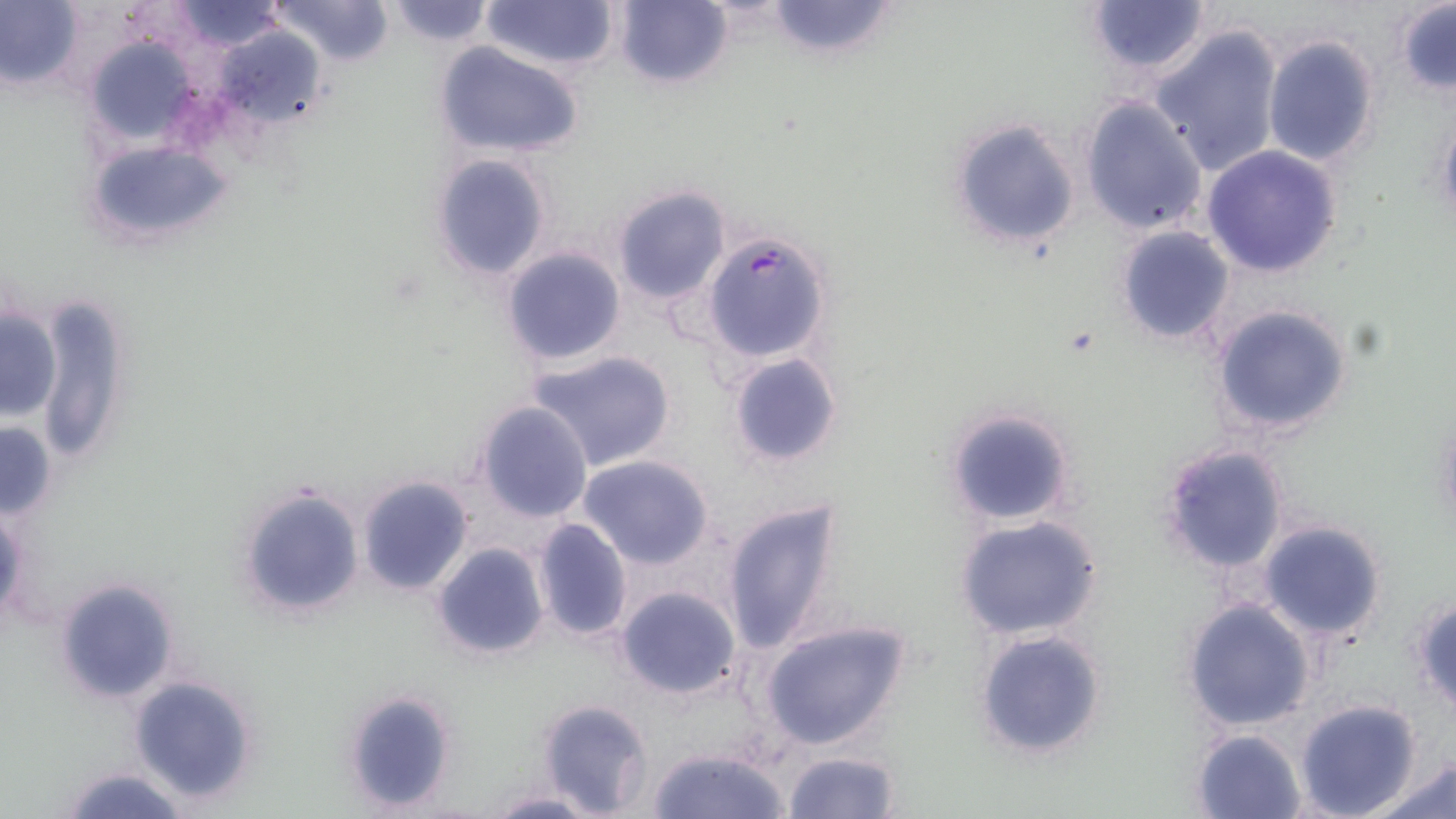

{
  "slide_level_diagnosis": "Plasmodium falciparum",
  "uninfected_red_blood_cell_locations": "approximate bounding boxes as (x1, y1, x2, y2) in pixels: (168, 0, 289, 53), (268, 0, 397, 68), (385, 0, 494, 47), (478, 0, 621, 72), (612, 0, 732, 89), (761, 0, 902, 60), (0, 1, 83, 90), (1084, 2, 1214, 80), (1394, 2, 1456, 93), (1151, 25, 1283, 175), (211, 26, 328, 124), (80, 34, 197, 146), (1261, 34, 1381, 169), (434, 43, 584, 159), (1079, 97, 1209, 237), (1433, 105, 1456, 229), (945, 116, 1082, 253), (85, 140, 234, 248), (1201, 146, 1344, 278), (430, 152, 553, 282), (612, 185, 731, 305), (1114, 225, 1236, 345), (501, 247, 627, 366), (33, 294, 135, 469), (1208, 303, 1356, 438), (0, 308, 61, 421), (527, 349, 677, 470), (726, 352, 844, 467), (476, 400, 593, 521), (941, 405, 1076, 530), (0, 418, 57, 522), (1157, 442, 1290, 577), (577, 454, 714, 570), (357, 475, 474, 596), (237, 486, 366, 619), (719, 495, 847, 657), (1, 505, 27, 623), (954, 515, 1103, 642), (532, 516, 632, 641), (1259, 519, 1388, 644), (431, 542, 549, 661), (55, 576, 179, 703), (615, 585, 741, 698), (1412, 594, 1456, 716), (1180, 597, 1317, 732), (759, 619, 911, 752), (974, 629, 1108, 760), (127, 674, 261, 805), (338, 688, 459, 813), (1294, 698, 1425, 819), (536, 699, 654, 817), (1190, 728, 1308, 819), (648, 745, 789, 819), (782, 749, 900, 819), (1370, 753, 1456, 819), (58, 765, 190, 819), (483, 790, 600, 817)",
  "stain": "May-Grünwald-Giemsa",
  "plasmodium_falciparum_infected_red_blood_cell_locations": "approximate bounding boxes as (x1, y1, x2, y2) in pixels: (702, 231, 832, 364)",
  "field_of_view": "one of a larger specimen",
  "image_size": "1456×819 pixels",
  "preparation": "thin blood film",
  "modality": "optical microscopy",
  "magnification": "1000x"
}